Assess this cell for malaria.
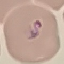

Parasitized.

Giemsa-stained preparation. Photographed with a smartphone camera at the microscope eyepiece. Thin blood film. Automatically extracted cell patch, resized to 64 × 64 pixels.